Give the preparation type.
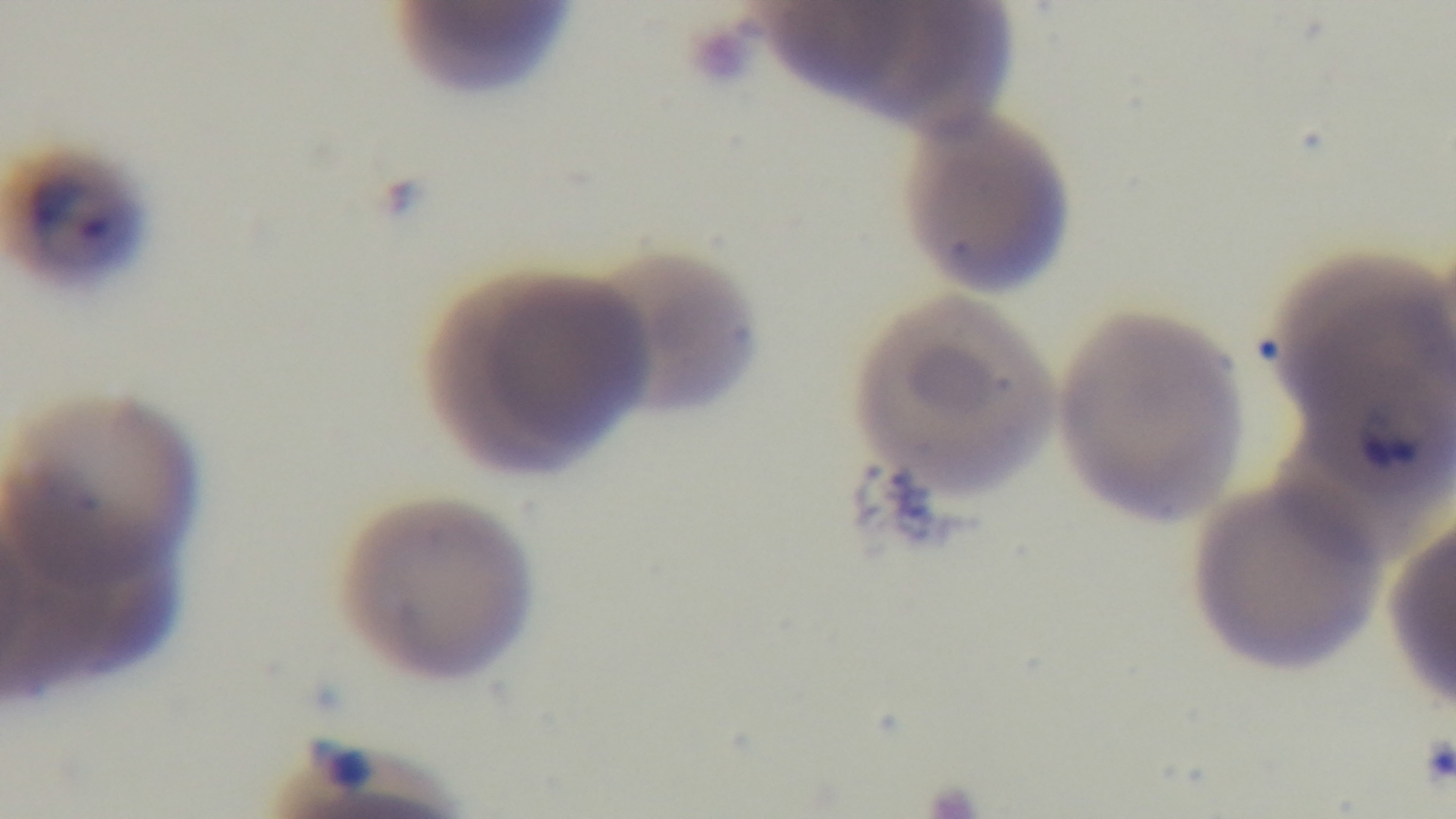

A thin smear.

One field from the slide. Captured with a mounted 4K digital camera. Giemsa stain. Oil-immersion objective, 100x. Malaria status: positive. Light microscopy.